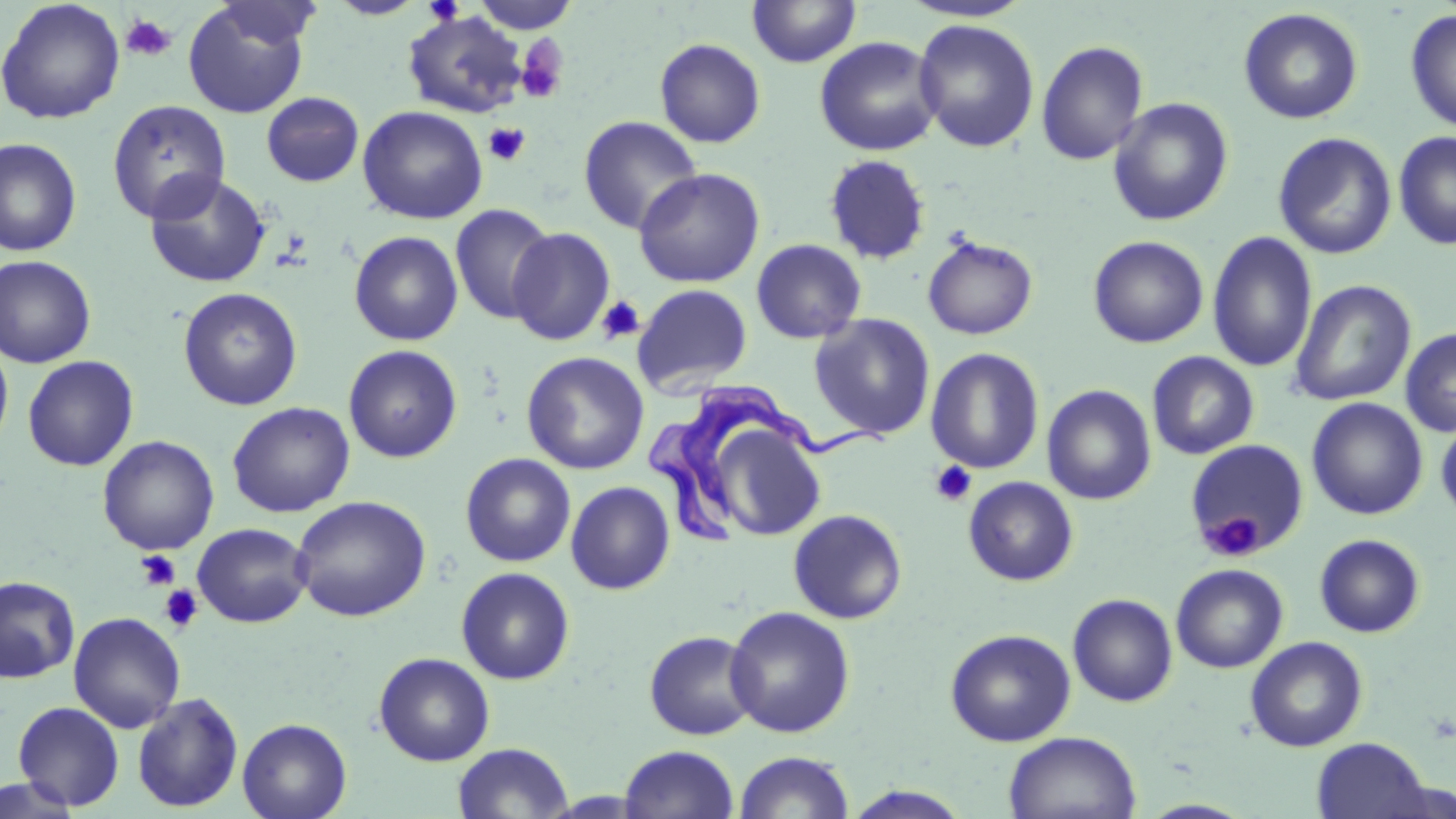

slide-level diagnosis = Trypanosoma brucei
modality = optical microscopy
stain = May-Grünwald-Giemsa
Trypanosoma brucei locations = approximate bounding boxes as (x1, y1, x2, y2) in pixels: (651, 380, 886, 548)
magnification = 1000x
platelet locations = approximate bounding boxes as (x1, y1, x2, y2) in pixels: (119, 14, 177, 62), (515, 37, 568, 105), (484, 123, 530, 167), (596, 295, 645, 346), (929, 460, 978, 507), (1202, 510, 1267, 560), (134, 550, 181, 590), (159, 585, 204, 633)
image size = 1456×819 pixels
uninfected red blood cell locations = approximate bounding boxes as (x1, y1, x2, y2) in pixels: (0, 0, 126, 124), (326, 0, 428, 19), (471, 0, 580, 34), (747, 0, 862, 68), (182, 1, 312, 118), (898, 1, 1035, 23), (1238, 7, 1364, 124), (1404, 8, 1456, 133), (402, 11, 529, 118), (913, 18, 1040, 152), (814, 36, 943, 156), (654, 38, 766, 148), (1035, 40, 1149, 166), (261, 92, 364, 186), (1107, 97, 1234, 227), (107, 99, 231, 223), (357, 105, 488, 225), (578, 115, 703, 235), (1393, 131, 1456, 250), (1273, 132, 1397, 260), (0, 137, 82, 256), (823, 154, 931, 265), (633, 168, 765, 288), (144, 171, 271, 288), (450, 203, 555, 325), (508, 227, 615, 346), (348, 230, 464, 345), (1207, 231, 1318, 373), (922, 235, 1038, 340), (1087, 235, 1209, 348), (750, 239, 867, 344), (0, 255, 96, 368), (1291, 280, 1416, 406), (632, 284, 752, 394), (178, 287, 303, 411), (809, 313, 936, 440), (1399, 327, 1456, 437), (0, 337, 14, 455), (343, 344, 463, 463), (925, 347, 1045, 474), (521, 351, 649, 475), (1146, 351, 1260, 460), (22, 355, 139, 470), (1042, 384, 1157, 505), (1306, 397, 1428, 520), (227, 401, 355, 517), (1435, 414, 1456, 524), (716, 429, 822, 538), (97, 435, 219, 555), (1184, 439, 1309, 556), (460, 452, 576, 567), (963, 476, 1079, 586), (566, 481, 676, 594), (290, 495, 431, 622), (788, 508, 908, 624), (192, 523, 313, 627), (1314, 533, 1426, 638), (1171, 563, 1289, 673), (455, 567, 575, 685), (0, 575, 80, 684), (1067, 593, 1178, 707), (724, 605, 856, 738), (68, 612, 185, 733), (945, 628, 1076, 746), (644, 630, 761, 740), (1245, 635, 1368, 752), (374, 652, 495, 766), (132, 691, 244, 813), (12, 701, 125, 811), (237, 717, 353, 819), (1003, 731, 1141, 819), (1311, 737, 1433, 819), (452, 742, 574, 819), (618, 745, 739, 819), (733, 751, 855, 818), (0, 775, 83, 818), (842, 786, 973, 819), (1137, 799, 1255, 818)
preparation = thin blood smear
field of view = one of a larger specimen